Classify this cell by malaria status.
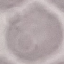

It is uninfected.

Thin blood film. Photographed with a smartphone camera at the microscope eyepiece. Giemsa stain. Automatically extracted cell patch, resized to 64 × 64 pixels.